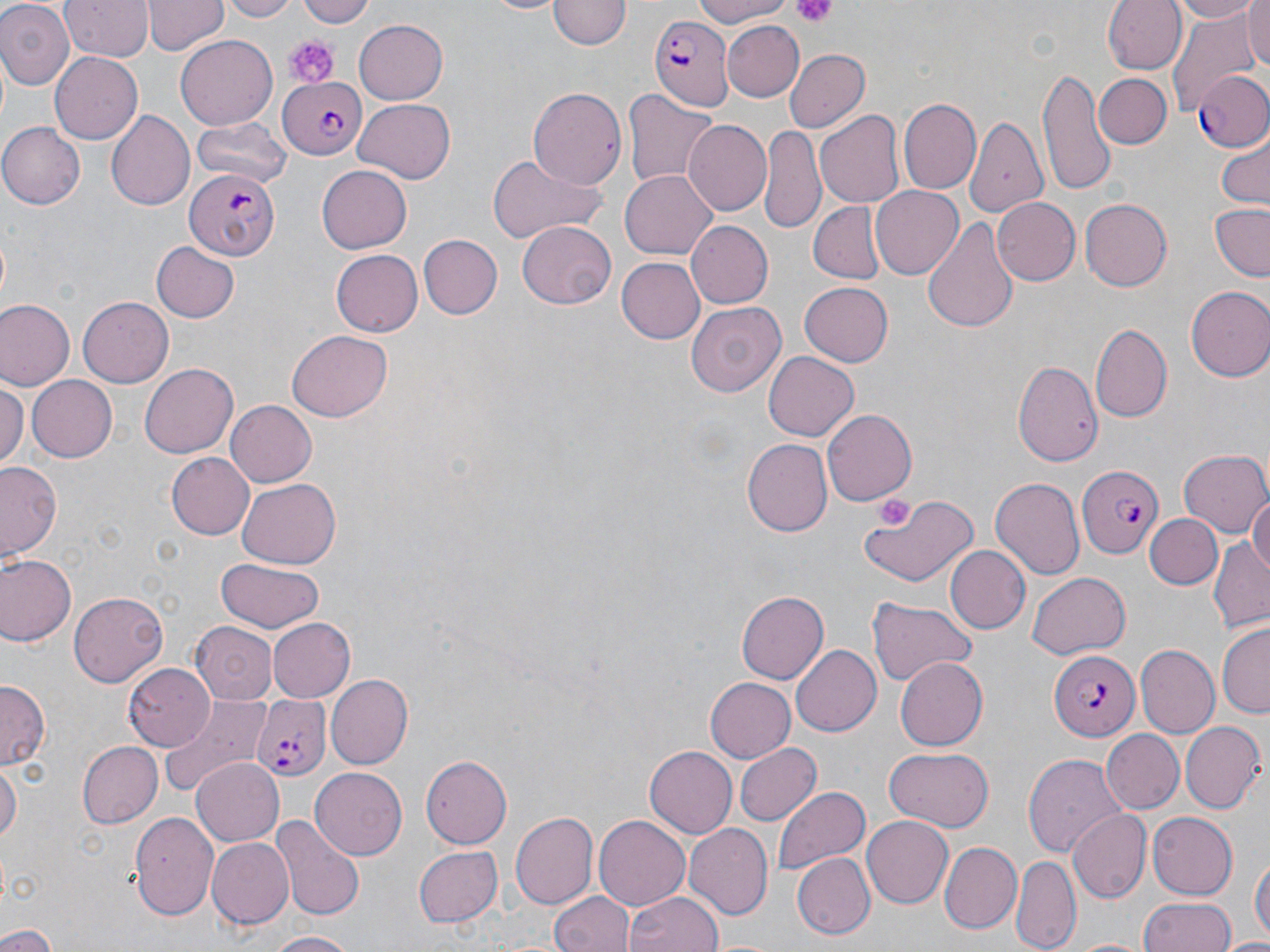 Approximate bounding boxes as named x1/y1/x2/y2 corners in pixels. Platelet locations: (x1=789, y1=0, x2=839, y2=26), (x1=281, y1=32, x2=339, y2=88). Plasmodium falciparum-infected red blood cell locations: (x1=648, y1=15, x2=733, y2=110), (x1=1191, y1=70, x2=1269, y2=152), (x1=278, y1=76, x2=369, y2=158), (x1=184, y1=166, x2=278, y2=260), (x1=1078, y1=462, x2=1165, y2=559), (x1=1050, y1=652, x2=1140, y2=738), (x1=248, y1=695, x2=333, y2=783). Uninfected red blood cell locations: (x1=60, y1=0, x2=152, y2=62), (x1=144, y1=0, x2=227, y2=56), (x1=222, y1=0, x2=301, y2=21), (x1=297, y1=0, x2=379, y2=27), (x1=483, y1=0, x2=568, y2=16), (x1=686, y1=0, x2=796, y2=26), (x1=1104, y1=0, x2=1188, y2=75), (x1=1166, y1=0, x2=1264, y2=24), (x1=550, y1=1, x2=627, y2=52), (x1=0, y1=2, x2=73, y2=87), (x1=1240, y1=2, x2=1269, y2=74), (x1=1165, y1=8, x2=1261, y2=117), (x1=354, y1=20, x2=450, y2=103), (x1=721, y1=21, x2=805, y2=100), (x1=177, y1=35, x2=278, y2=128), (x1=783, y1=48, x2=869, y2=132), (x1=49, y1=53, x2=143, y2=142), (x1=1037, y1=64, x2=1117, y2=198), (x1=1094, y1=73, x2=1172, y2=150), (x1=529, y1=86, x2=627, y2=193), (x1=623, y1=90, x2=718, y2=193), (x1=355, y1=97, x2=454, y2=181), (x1=899, y1=97, x2=981, y2=194), (x1=816, y1=108, x2=904, y2=208), (x1=106, y1=109, x2=194, y2=210), (x1=193, y1=115, x2=290, y2=188), (x1=965, y1=117, x2=1050, y2=219), (x1=683, y1=118, x2=773, y2=215), (x1=0, y1=123, x2=85, y2=208), (x1=759, y1=125, x2=826, y2=232), (x1=1214, y1=136, x2=1269, y2=210), (x1=485, y1=153, x2=608, y2=243), (x1=316, y1=166, x2=412, y2=253), (x1=620, y1=169, x2=718, y2=260), (x1=869, y1=186, x2=963, y2=281), (x1=993, y1=198, x2=1080, y2=287), (x1=1081, y1=198, x2=1171, y2=291), (x1=810, y1=202, x2=886, y2=282), (x1=1208, y1=204, x2=1270, y2=282), (x1=921, y1=216, x2=1019, y2=332), (x1=686, y1=220, x2=775, y2=308), (x1=518, y1=222, x2=615, y2=309), (x1=417, y1=234, x2=501, y2=320), (x1=152, y1=243, x2=238, y2=321), (x1=330, y1=249, x2=423, y2=336), (x1=615, y1=256, x2=703, y2=341), (x1=800, y1=282, x2=893, y2=367), (x1=1186, y1=286, x2=1270, y2=381), (x1=77, y1=296, x2=173, y2=388), (x1=0, y1=300, x2=74, y2=390), (x1=686, y1=301, x2=787, y2=398), (x1=1090, y1=321, x2=1172, y2=422), (x1=288, y1=330, x2=392, y2=421), (x1=764, y1=353, x2=858, y2=439), (x1=1014, y1=360, x2=1103, y2=467), (x1=137, y1=364, x2=238, y2=459), (x1=26, y1=375, x2=117, y2=462), (x1=0, y1=382, x2=27, y2=467), (x1=227, y1=400, x2=316, y2=486), (x1=821, y1=410, x2=915, y2=505), (x1=740, y1=439, x2=832, y2=537), (x1=1178, y1=449, x2=1269, y2=538), (x1=167, y1=453, x2=255, y2=540), (x1=0, y1=461, x2=65, y2=561), (x1=991, y1=477, x2=1084, y2=580), (x1=235, y1=478, x2=342, y2=568), (x1=860, y1=494, x2=979, y2=591), (x1=1248, y1=494, x2=1270, y2=579), (x1=1144, y1=512, x2=1223, y2=589), (x1=1208, y1=540, x2=1269, y2=632), (x1=946, y1=547, x2=1030, y2=634), (x1=2, y1=553, x2=76, y2=645), (x1=215, y1=557, x2=327, y2=632), (x1=1027, y1=572, x2=1130, y2=658), (x1=737, y1=590, x2=829, y2=683), (x1=70, y1=592, x2=167, y2=687), (x1=867, y1=595, x2=980, y2=686), (x1=266, y1=617, x2=355, y2=703), (x1=190, y1=619, x2=277, y2=701), (x1=1218, y1=623, x2=1269, y2=719), (x1=789, y1=644, x2=880, y2=737), (x1=1136, y1=646, x2=1218, y2=739), (x1=896, y1=658, x2=988, y2=750), (x1=123, y1=662, x2=215, y2=747), (x1=326, y1=675, x2=412, y2=770), (x1=706, y1=676, x2=797, y2=762), (x1=0, y1=683, x2=48, y2=770), (x1=161, y1=698, x2=271, y2=797), (x1=1180, y1=722, x2=1264, y2=813), (x1=1101, y1=729, x2=1185, y2=813), (x1=75, y1=740, x2=162, y2=830), (x1=733, y1=742, x2=818, y2=826), (x1=644, y1=744, x2=737, y2=835), (x1=884, y1=748, x2=996, y2=831), (x1=1024, y1=753, x2=1125, y2=859), (x1=420, y1=755, x2=512, y2=848), (x1=191, y1=757, x2=286, y2=846), (x1=0, y1=763, x2=20, y2=848), (x1=310, y1=767, x2=407, y2=860), (x1=773, y1=786, x2=870, y2=876), (x1=1066, y1=810, x2=1149, y2=903), (x1=127, y1=811, x2=220, y2=919), (x1=511, y1=811, x2=598, y2=910), (x1=1146, y1=813, x2=1238, y2=900), (x1=594, y1=816, x2=690, y2=911), (x1=862, y1=817, x2=953, y2=906), (x1=277, y1=819, x2=366, y2=921), (x1=685, y1=825, x2=773, y2=916), (x1=205, y1=838, x2=293, y2=928), (x1=938, y1=842, x2=1020, y2=933), (x1=413, y1=846, x2=503, y2=928), (x1=790, y1=852, x2=875, y2=939), (x1=1250, y1=854, x2=1268, y2=949), (x1=1012, y1=855, x2=1081, y2=951), (x1=549, y1=889, x2=636, y2=952), (x1=625, y1=893, x2=723, y2=952), (x1=1138, y1=897, x2=1239, y2=951), (x1=0, y1=925, x2=56, y2=952), (x1=264, y1=932, x2=359, y2=952), (x1=1070, y1=937, x2=1148, y2=952), (x1=1225, y1=938, x2=1270, y2=952). Slide-level diagnosis: Plasmodium falciparum. Optical microscopy. May-Grünwald-Giemsa-stained preparation. One field of a larger specimen. 1000x magnification. Thin blood smear. Image is 1270×952 pixels.